Give the position of every Plasmodium parasite.
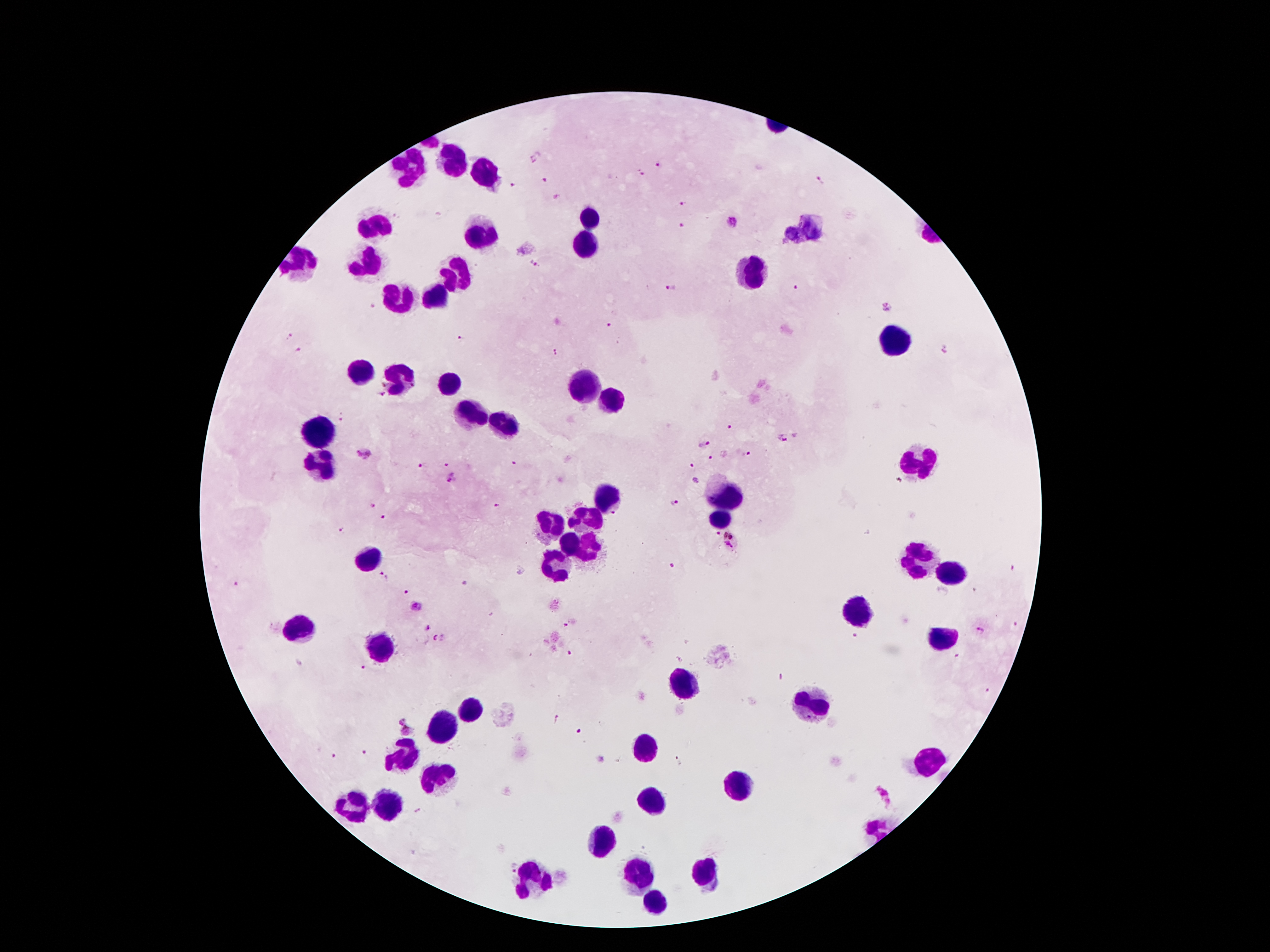
Approximate object centers, in pixels from the top-left corner.
Plasmodium parasites: (x=536, y=157), (x=658, y=165), (x=640, y=174), (x=544, y=180), (x=821, y=180), (x=513, y=186), (x=556, y=197), (x=683, y=204), (x=733, y=224), (x=681, y=226), (x=535, y=265), (x=797, y=287), (x=670, y=289), (x=374, y=307), (x=887, y=307), (x=609, y=325), (x=290, y=336), (x=460, y=338), (x=298, y=351), (x=557, y=352), (x=342, y=420), (x=730, y=428), (x=782, y=439), (x=703, y=443), (x=747, y=454), (x=364, y=456), (x=710, y=459), (x=515, y=462), (x=446, y=463), (x=421, y=466), (x=691, y=467), (x=454, y=479), (x=695, y=481), (x=372, y=504), (x=674, y=504), (x=495, y=506), (x=383, y=518), (x=341, y=529), (x=715, y=534), (x=732, y=542), (x=671, y=565), (x=1013, y=569), (x=520, y=571), (x=385, y=576), (x=237, y=584), (x=465, y=585), (x=974, y=590), (x=405, y=592), (x=416, y=606), (x=1014, y=625), (x=565, y=626), (x=428, y=628), (x=982, y=631), (x=854, y=637), (x=439, y=638), (x=569, y=653), (x=955, y=657), (x=363, y=668), (x=989, y=690), (x=403, y=719), (x=557, y=719), (x=407, y=731), (x=580, y=731), (x=364, y=753), (x=332, y=757), (x=678, y=763), (x=885, y=795), (x=510, y=866).

Leukocyte locations: (x=456, y=164), (x=411, y=167), (x=486, y=175), (x=590, y=220), (x=372, y=222), (x=803, y=231), (x=479, y=236), (x=586, y=243), (x=302, y=260), (x=368, y=263), (x=456, y=272), (x=753, y=274), (x=438, y=296), (x=399, y=302), (x=895, y=344), (x=360, y=371), (x=398, y=380), (x=447, y=385), (x=580, y=388), (x=610, y=402), (x=470, y=414), (x=500, y=426), (x=319, y=431), (x=323, y=463), (x=922, y=464), (x=607, y=500), (x=730, y=501), (x=586, y=521), (x=718, y=523), (x=547, y=525), (x=571, y=543), (x=590, y=546), (x=368, y=560), (x=914, y=561), (x=558, y=567), (x=946, y=575), (x=861, y=610), (x=295, y=627), (x=945, y=639), (x=380, y=646), (x=683, y=685), (x=813, y=706), (x=470, y=709), (x=444, y=726), (x=644, y=748), (x=403, y=755), (x=927, y=762), (x=435, y=781), (x=737, y=786), (x=651, y=799), (x=354, y=807), (x=387, y=808), (x=603, y=840), (x=706, y=873), (x=638, y=875), (x=535, y=878), (x=655, y=901). Giemsa-stained preparation. Thick peripheral-blood smear. One field from this slide. Photographed through the microscope eyepiece with a smartphone camera. Patient malaria status: infected with Plasmodium falciparum. 100x magnification. Image is 1270×952 pixels.